Locate and identify every blood parasite.
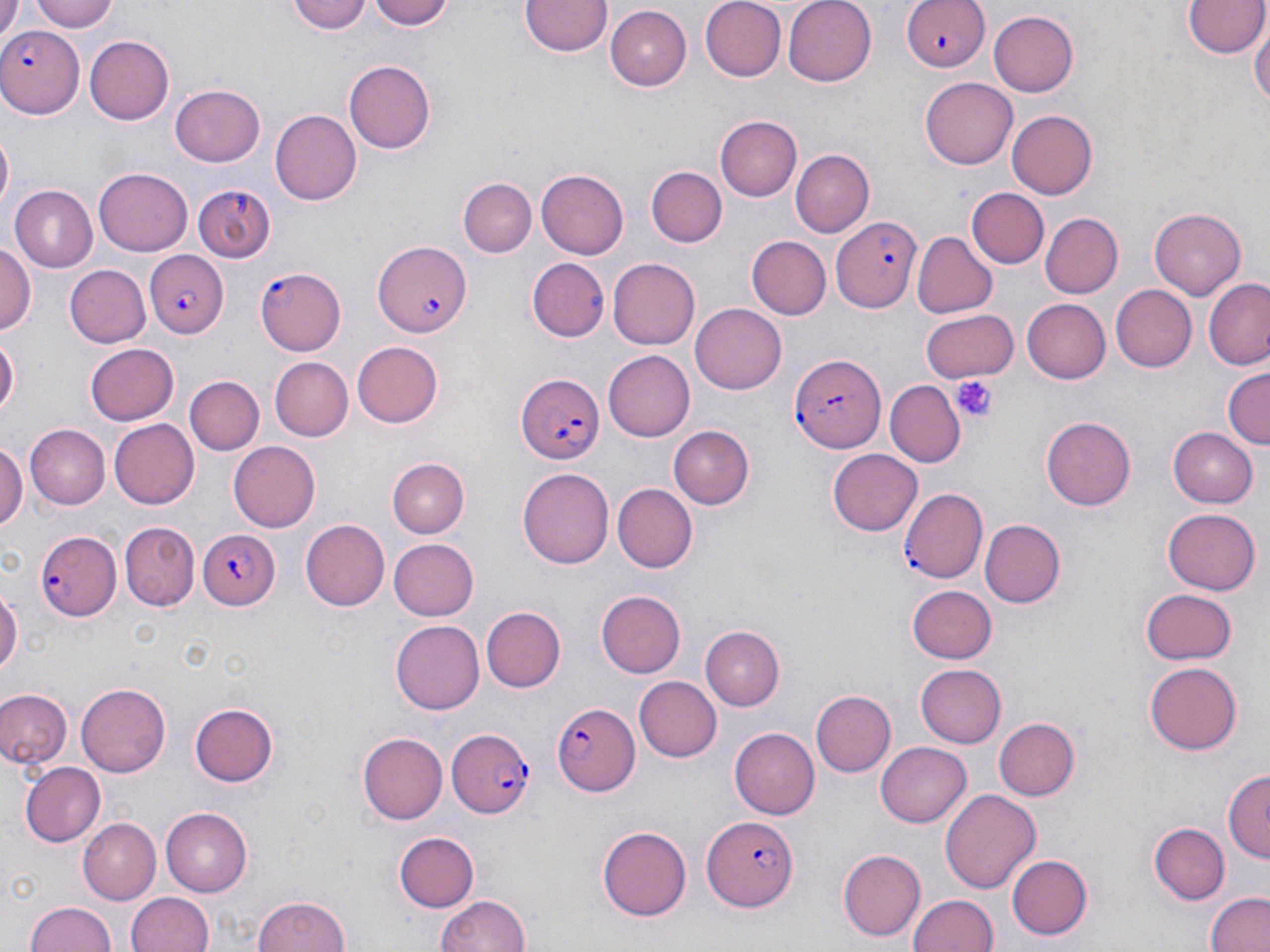
Approximate bounding boxes as (x1, y1, x2, y2) in pixels.
Plasmodium falciparum-infected red blood cells: (898, 0, 990, 73), (0, 25, 83, 117), (832, 215, 920, 311), (372, 240, 474, 335), (143, 251, 227, 338), (256, 266, 346, 355), (790, 354, 884, 451), (516, 373, 606, 466), (899, 486, 987, 584), (34, 526, 123, 621), (198, 528, 280, 607), (550, 702, 641, 793), (446, 726, 535, 818), (705, 814, 798, 911).
No Plasmodium ovale, Plasmodium malariae, Plasmodium vivax, Babesia divergens, or Trypanosoma brucei observed.

Platelet locations: (953, 375, 997, 424). Uninfected red blood cell locations: (28, 0, 122, 32), (288, 0, 372, 34), (370, 0, 454, 31), (518, 0, 612, 58), (699, 0, 785, 82), (782, 0, 878, 87), (1184, 1, 1265, 59), (0, 3, 28, 50), (522, 4, 687, 69), (605, 6, 690, 90), (990, 10, 1079, 97), (1250, 19, 1270, 115), (85, 36, 174, 124), (343, 59, 435, 154), (921, 76, 1020, 168), (171, 84, 265, 166), (270, 108, 362, 206), (1007, 110, 1097, 199), (714, 116, 800, 202), (1, 132, 14, 211), (790, 149, 874, 235), (96, 165, 195, 255), (647, 167, 727, 247), (536, 169, 629, 258), (461, 177, 536, 258), (192, 183, 275, 261), (9, 186, 98, 273), (966, 188, 1049, 269), (1150, 205, 1246, 297), (1041, 213, 1122, 297), (913, 231, 995, 318), (747, 236, 830, 319), (0, 243, 36, 335), (526, 258, 610, 343), (607, 259, 701, 348), (65, 266, 149, 348), (1204, 279, 1270, 370), (1108, 285, 1197, 372), (1024, 298, 1111, 383), (691, 302, 786, 391), (918, 307, 1017, 383), (0, 333, 19, 424), (351, 342, 444, 427), (86, 343, 180, 424), (603, 352, 694, 439), (268, 356, 352, 441), (1222, 368, 1269, 452), (186, 376, 264, 454), (886, 382, 966, 467), (1041, 416, 1134, 510), (109, 419, 199, 509), (25, 425, 109, 508), (668, 425, 753, 511), (1169, 427, 1257, 506), (0, 440, 25, 534), (229, 441, 321, 533), (828, 450, 923, 535), (387, 458, 467, 538), (518, 467, 614, 571), (614, 485, 697, 574), (1163, 508, 1260, 596), (300, 519, 389, 611), (978, 519, 1065, 609), (121, 521, 198, 610), (389, 538, 479, 619), (0, 585, 20, 681), (907, 585, 996, 663), (1142, 588, 1237, 664), (596, 590, 685, 678), (481, 606, 566, 692), (391, 618, 483, 712), (701, 626, 783, 709), (914, 663, 1006, 747), (1146, 663, 1244, 755), (633, 676, 719, 761), (75, 683, 169, 776), (1, 689, 71, 766), (812, 691, 896, 776), (188, 702, 276, 788), (995, 716, 1081, 798), (729, 727, 819, 820), (358, 732, 447, 824), (875, 741, 971, 828), (21, 764, 106, 848), (1223, 772, 1269, 863), (940, 786, 1040, 890), (162, 807, 252, 895), (77, 817, 160, 903), (597, 823, 690, 919), (1149, 823, 1228, 902), (393, 831, 479, 914), (838, 849, 925, 940), (1008, 854, 1092, 939), (1203, 891, 1270, 952), (125, 892, 216, 951), (908, 893, 998, 952), (251, 894, 351, 952), (434, 894, 532, 952), (25, 900, 118, 951). Slide-level diagnosis: Plasmodium falciparum. Image is 1270×952 pixels. Optical microscopy. Single field of view. May-Grünwald-Giemsa-stained preparation. Thin blood film. 1000x magnification.